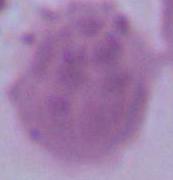

Summary:
  - Magnification: 1000x
  - Identification: red blood cell
  - Modality: photomicrograph